Give the position of every malaria parasite.
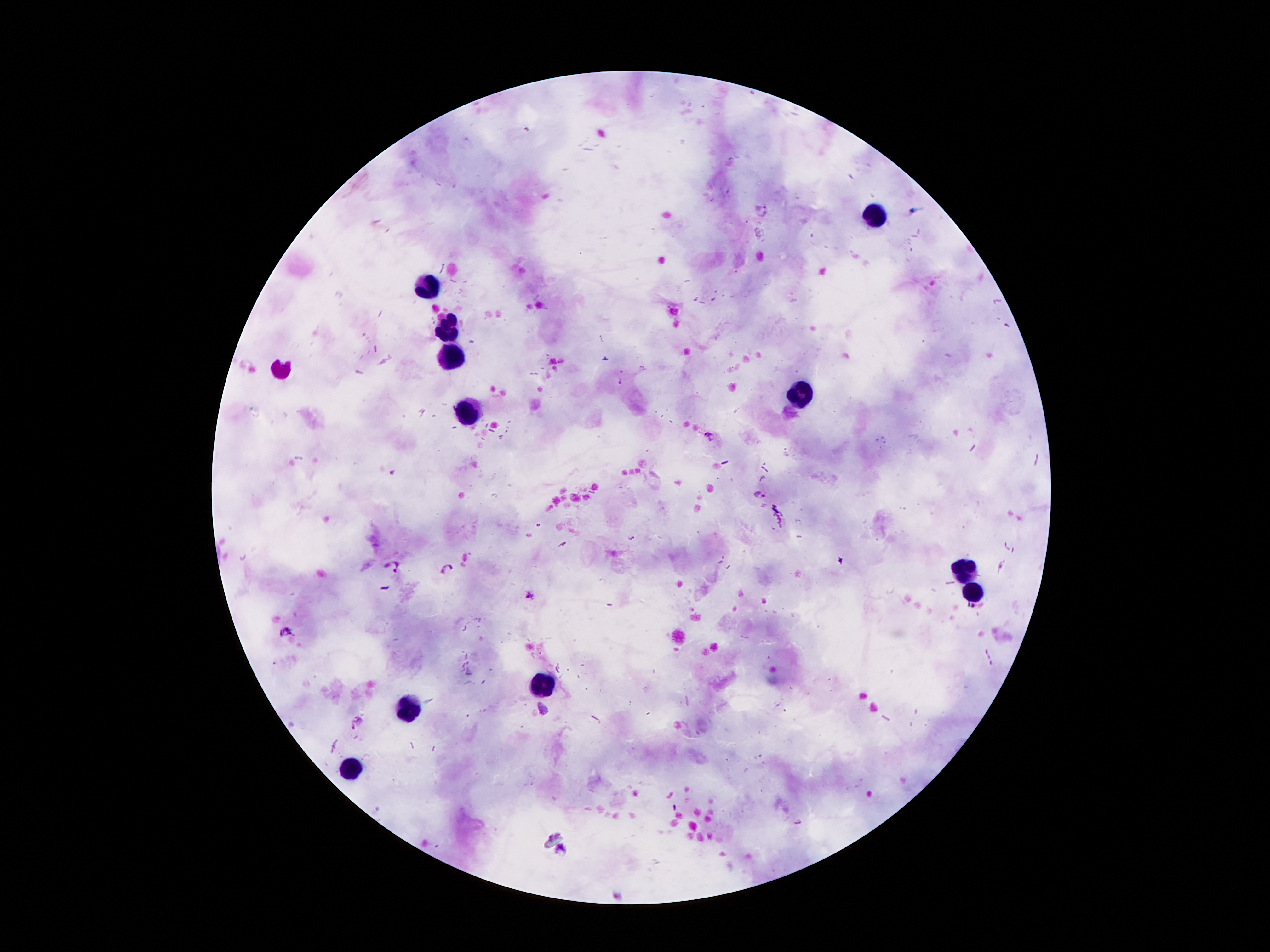

Approximate centers as {x, y} in pixels.
Malaria parasites: {762, 211}, {761, 494}, {392, 566}, {447, 567}, {532, 596}.

Leukocyte locations: {875, 212}, {429, 287}, {448, 325}, {452, 360}, {278, 373}, {804, 396}, {470, 413}, {962, 569}, {971, 594}, {540, 686}, {411, 709}, {352, 771}. Single field of view. Photographed through the microscope eyepiece with a smartphone camera. Giemsa stain. Thick peripheral-blood smear. Image is 1270×952 pixels. Patient malaria status: positive for Plasmodium falciparum. 100x magnification.